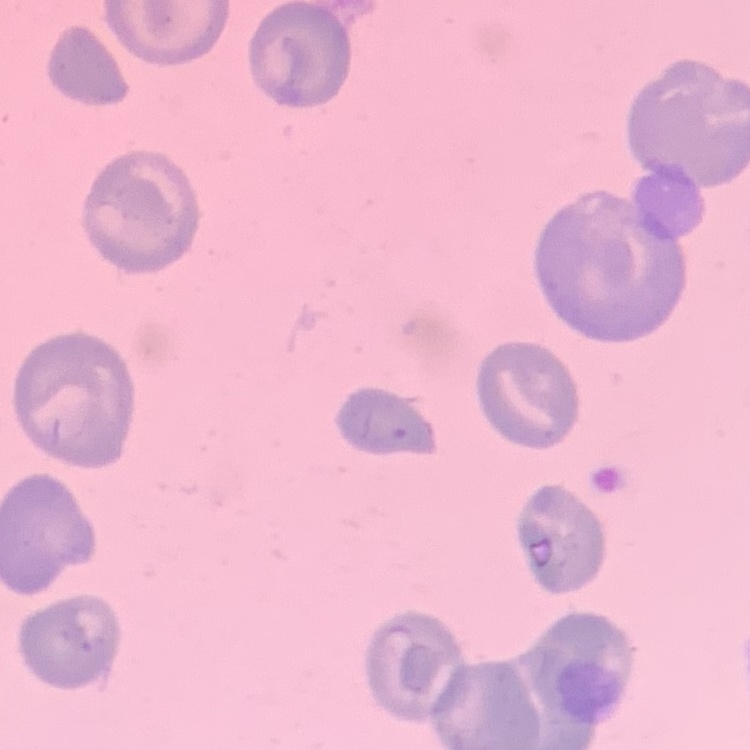
{
  "red_blood_cell_morphology": "no rouleaux formation",
  "image_type": "square crop of a larger photomicrograph",
  "stain": "Field's or Giemsa",
  "preparation": "thin peripheral smear"
}